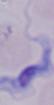 A trypanosome is shown. 1000x magnification. Photomicrograph.